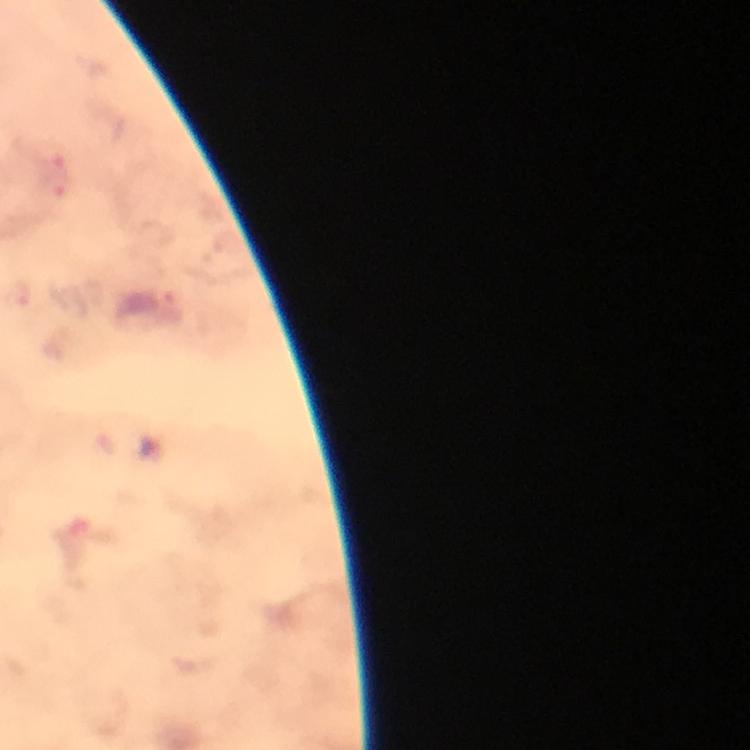

{
  "magnification": "100x",
  "stain": "Giemsa",
  "capture": "smartphone camera through the microscope",
  "malaria_parasite_locations": "approximate centers as (x, y) in pixels: (52, 155), (57, 184)",
  "cropped_from": "one field of view",
  "image_size": "750×750 pixels",
  "immersion_oil": "applied",
  "preparation": "thick blood smear",
  "context": "from a malaria diagnostic workup"
}